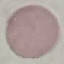
malaria status = uninfected
capture = smartphone through the microscope eyepiece
stain = Giemsa
preparation = thin blood smear
image type = automatically extracted cell patch, resized to 64 × 64 pixels